Report the malaria status of this cell.
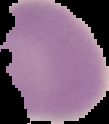

It is uninfected.

From a thin blood smear. Image is 109×124 pixels. Cell region segmented out of the field of view; the surrounding area is masked to black.